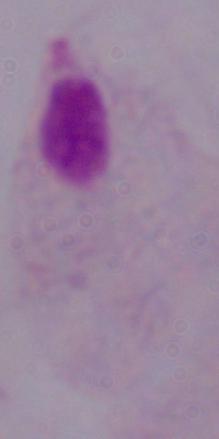
Summary:
  - Identification: trichomonad
  - Magnification: 1000x
  - Modality: micrograph